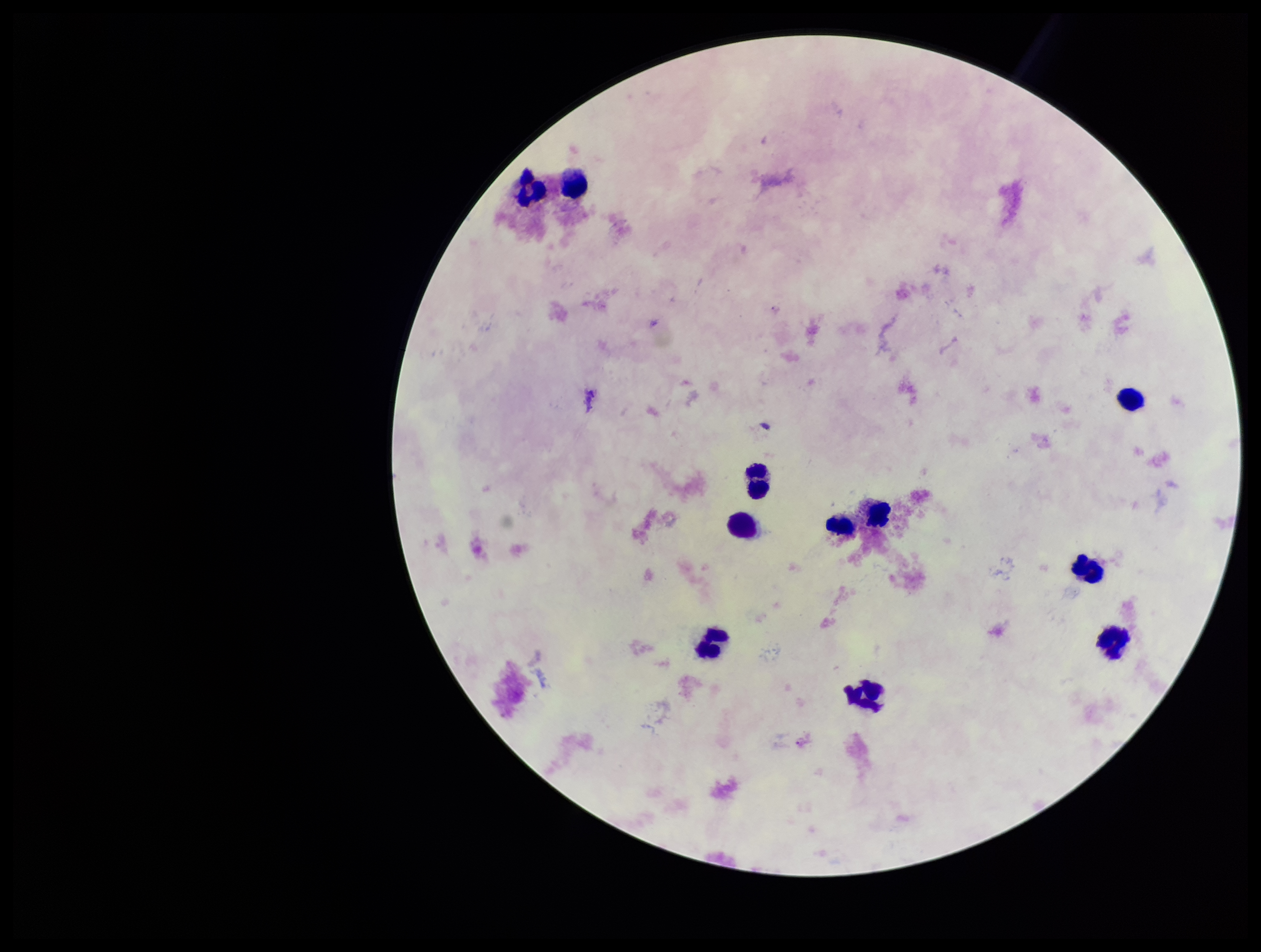
patient_malaria_status: negative
preparation: thick
field_of_view: single
capture: smartphone photograph through the microscope eyepiece
parasite_count: 0
leukocyte_count: 11
image_size: 1261×952 pixels
plasmodium_parasites: none detected
stain: Giemsa